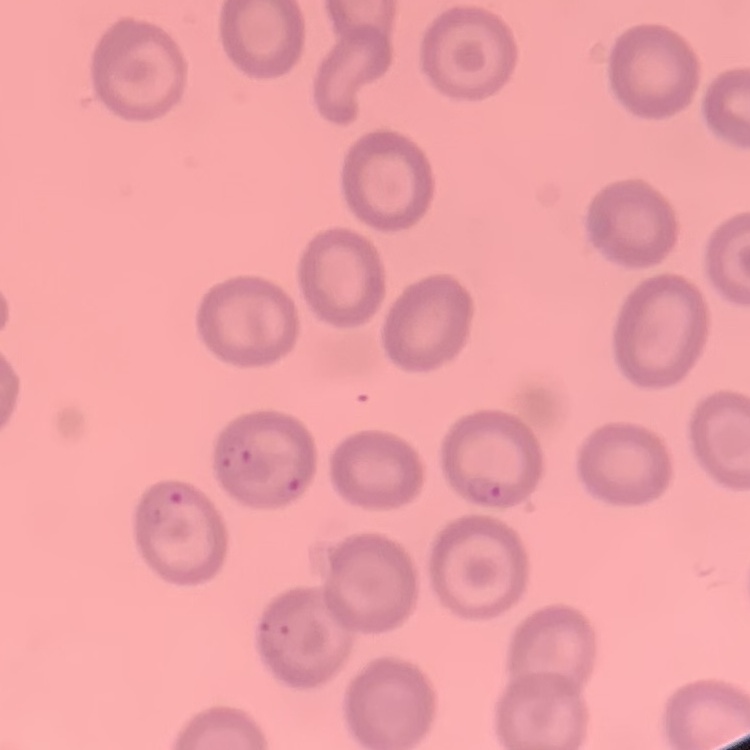 The red blood cells show no rouleaux formation. Thin blood film. Stained with either Field's or Giemsa. One tile cut from a larger photomicrograph.